State which parasite is depicted.
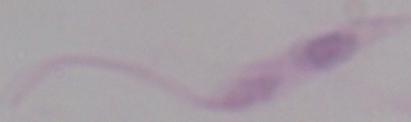
Leishmania.

modality = micrograph
magnification = 1000x